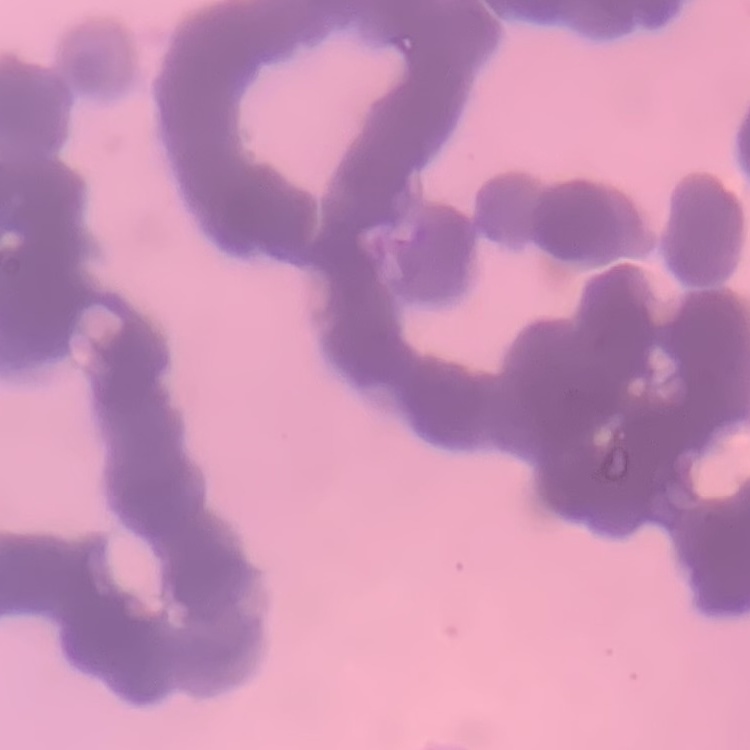
Summary:
  - Erythrocyte morphology: rouleaux formation
  - Preparation: thin blood smear
  - Image type: square crop of a larger photomicrograph
  - Stain: Field's or Giemsa